Give the position of every Plasmodium parasite visible.
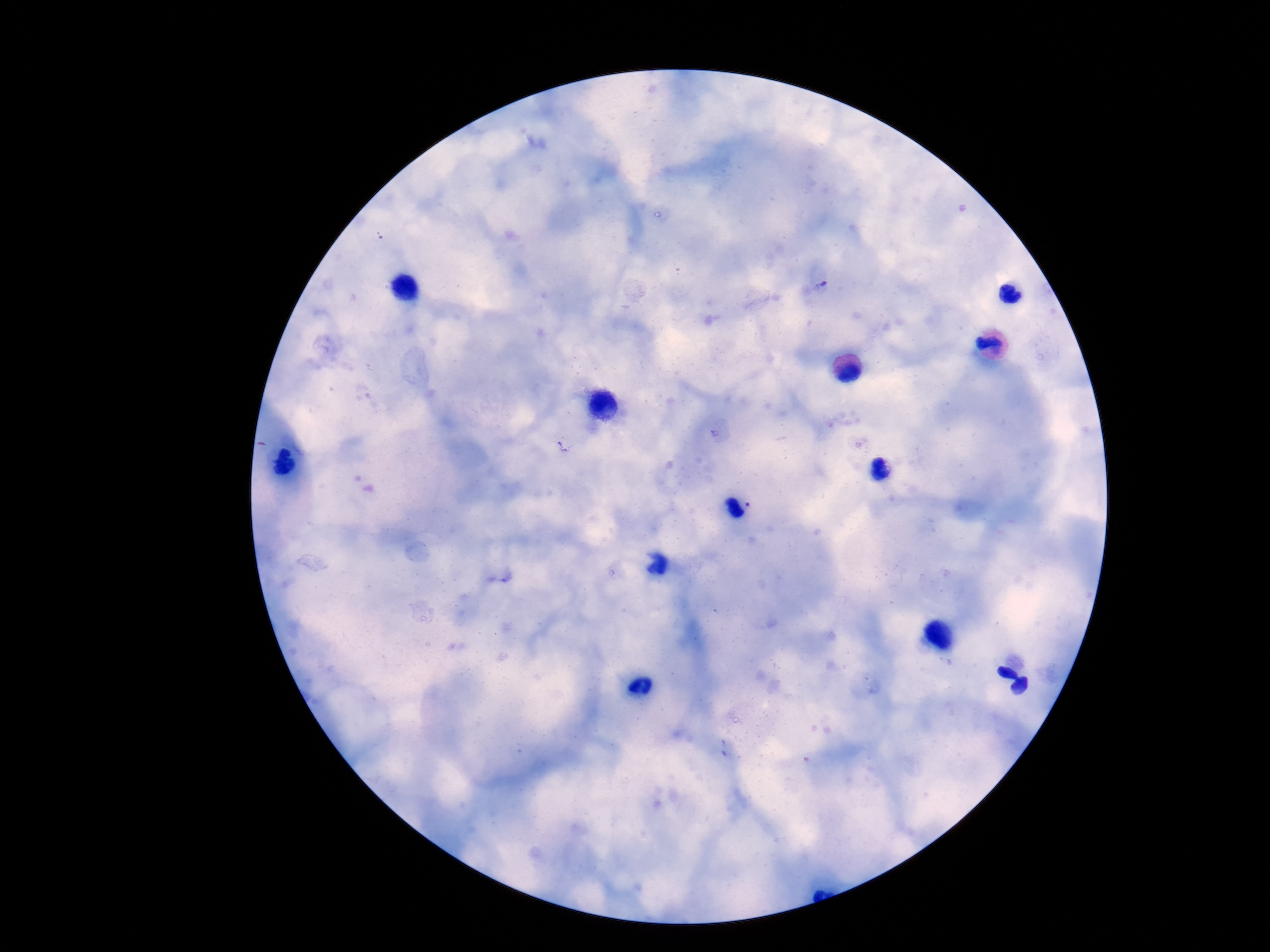

Approximate centers as [x, y] in pixels.
Plasmodium parasites: [821, 287], [563, 444].

Summary:
  - Preparation: thick blood smear
  - Magnification: 100x
  - Field of view: one from this slide
  - Image size: 1270×952 pixels
  - Stain: Giemsa
  - Patient malaria status: positive
  - Capture: smartphone camera through the microscope eyepiece